Give the position of every leukocyte visible.
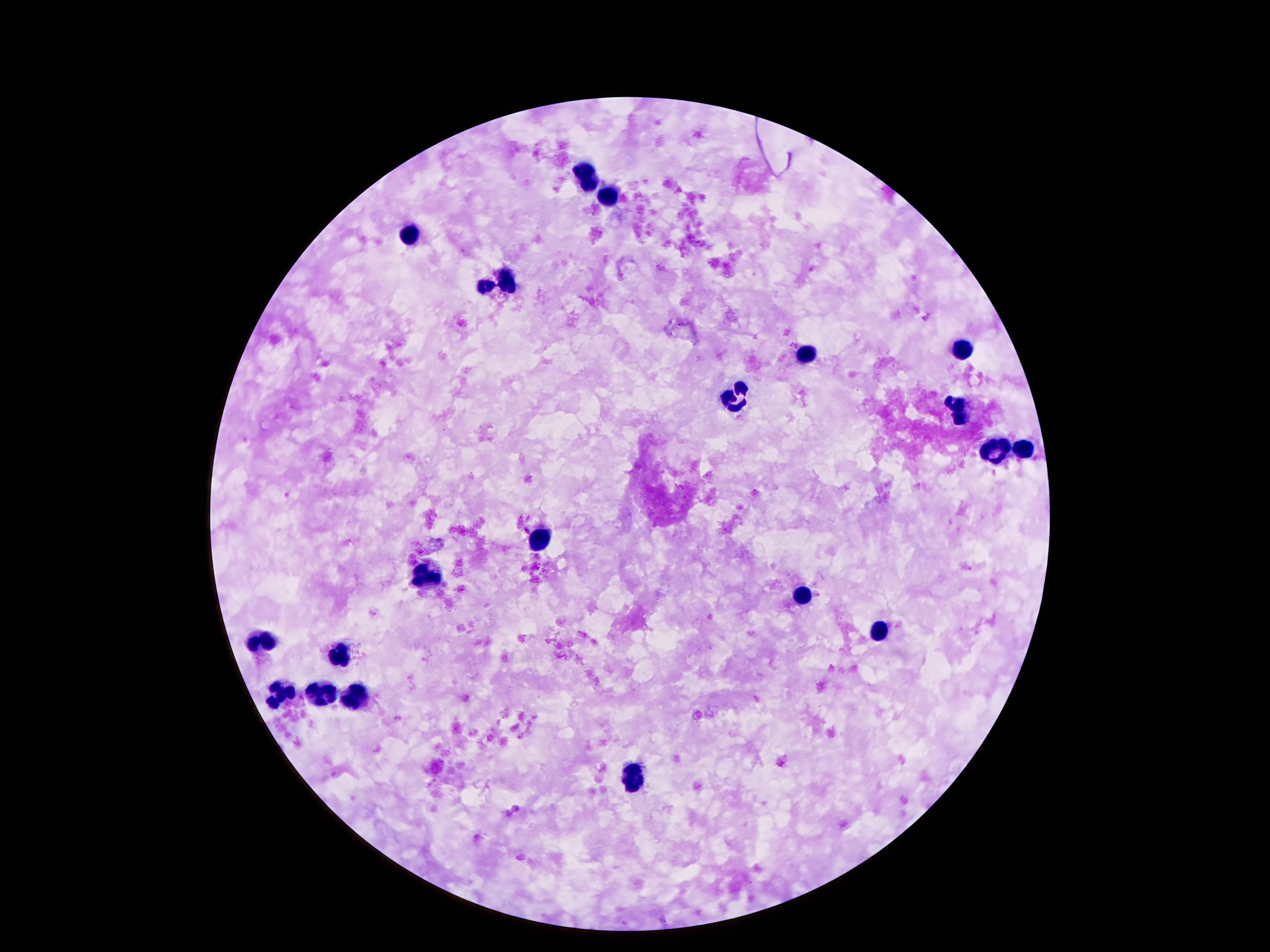
Approximate centers as [x, y] in pixels.
Leukocytes: [588, 173], [609, 199], [409, 234], [504, 278], [485, 284], [964, 348], [806, 354], [735, 400], [960, 408], [993, 451], [1023, 451], [538, 539], [424, 576], [800, 591], [878, 637], [256, 639], [336, 654], [281, 691], [321, 694], [353, 698], [630, 777].

Smartphone photograph taken through the microscope eyepiece. 100x magnification. Giemsa stain. Thick blood film. Patient malaria status: uninfected. Image is 1270×952 pixels. One field from this slide.